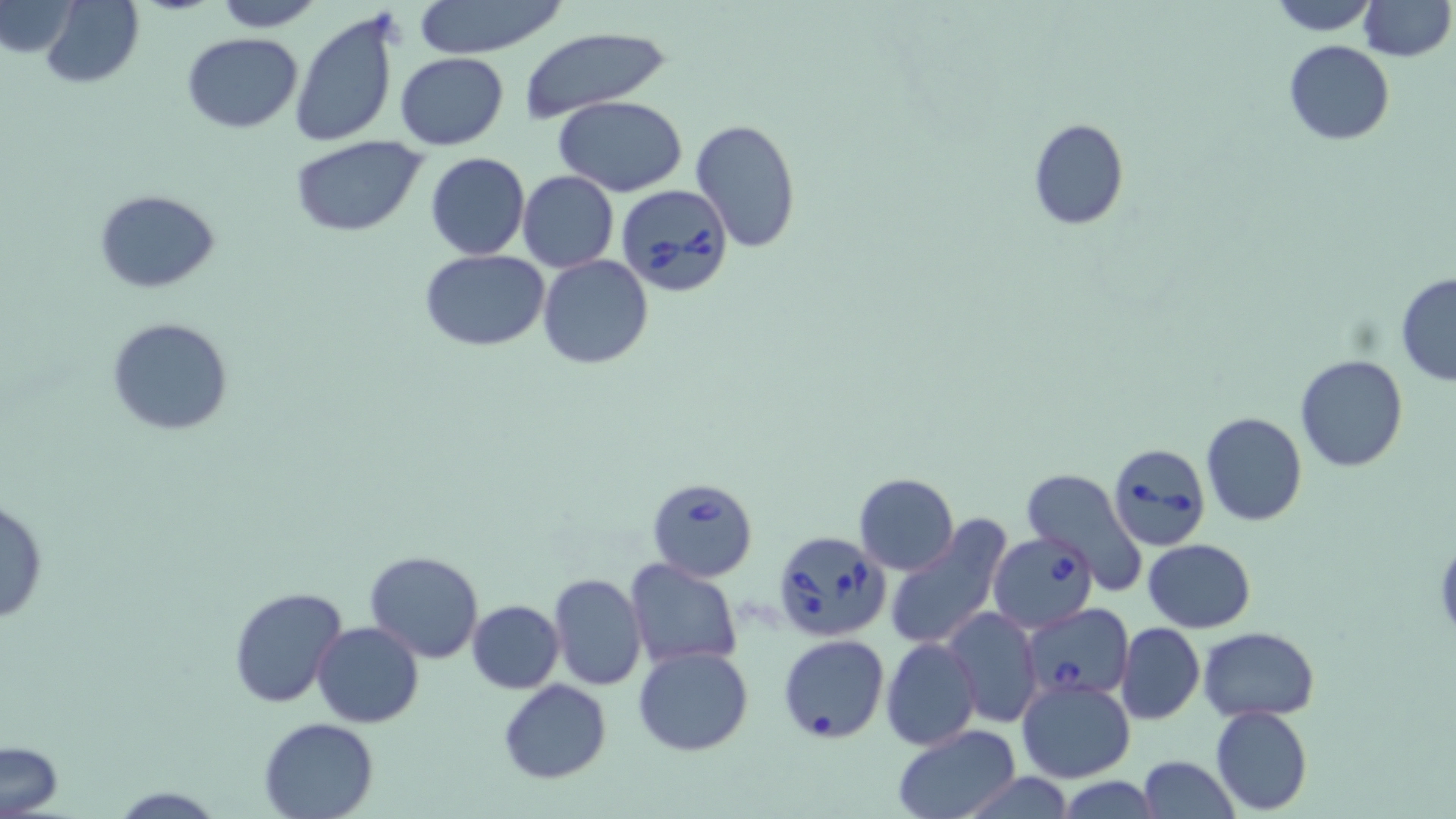

Approximate bounding boxes as named x1/y1/x2/y2 corners in pixels. Babesia divergens-infected red blood cell locations: (x1=614, y1=184, x2=734, y2=297), (x1=1107, y1=442, x2=1210, y2=551), (x1=646, y1=477, x2=758, y2=580), (x1=772, y1=529, x2=890, y2=641), (x1=987, y1=531, x2=1099, y2=634), (x1=1025, y1=602, x2=1137, y2=699). Uninfected red blood cell locations: (x1=0, y1=0, x2=78, y2=59), (x1=40, y1=0, x2=143, y2=89), (x1=210, y1=0, x2=325, y2=31), (x1=411, y1=0, x2=570, y2=58), (x1=1264, y1=0, x2=1380, y2=35), (x1=1357, y1=0, x2=1453, y2=61), (x1=289, y1=11, x2=400, y2=149), (x1=519, y1=29, x2=666, y2=119), (x1=183, y1=32, x2=302, y2=132), (x1=1282, y1=40, x2=1395, y2=145), (x1=395, y1=51, x2=509, y2=150), (x1=554, y1=96, x2=689, y2=198), (x1=1027, y1=117, x2=1128, y2=231), (x1=690, y1=118, x2=802, y2=252), (x1=290, y1=138, x2=425, y2=235), (x1=425, y1=151, x2=530, y2=259), (x1=518, y1=170, x2=620, y2=273), (x1=94, y1=191, x2=221, y2=292), (x1=419, y1=249, x2=550, y2=349), (x1=538, y1=254, x2=653, y2=369), (x1=1395, y1=275, x2=1456, y2=385), (x1=107, y1=317, x2=234, y2=437), (x1=1296, y1=356, x2=1407, y2=473), (x1=1201, y1=412, x2=1308, y2=527), (x1=1020, y1=469, x2=1148, y2=589), (x1=853, y1=473, x2=959, y2=574), (x1=0, y1=498, x2=49, y2=628), (x1=883, y1=517, x2=1012, y2=653), (x1=1435, y1=535, x2=1456, y2=644), (x1=1142, y1=539, x2=1255, y2=633), (x1=365, y1=549, x2=484, y2=664), (x1=625, y1=560, x2=742, y2=670), (x1=548, y1=573, x2=647, y2=691), (x1=227, y1=586, x2=348, y2=708), (x1=466, y1=598, x2=564, y2=693), (x1=942, y1=607, x2=1042, y2=729), (x1=312, y1=621, x2=423, y2=728), (x1=1117, y1=623, x2=1204, y2=724), (x1=1198, y1=627, x2=1321, y2=721), (x1=777, y1=633, x2=890, y2=744), (x1=882, y1=637, x2=981, y2=752), (x1=632, y1=645, x2=754, y2=755), (x1=1017, y1=677, x2=1135, y2=784), (x1=497, y1=680, x2=613, y2=784), (x1=1209, y1=705, x2=1312, y2=815), (x1=258, y1=716, x2=380, y2=819), (x1=890, y1=724, x2=1023, y2=819), (x1=1, y1=741, x2=65, y2=815), (x1=1137, y1=756, x2=1238, y2=817), (x1=111, y1=784, x2=223, y2=818). Slide-level diagnosis: Babesia divergens. Light microscopy. 1000x magnification. Thin blood smear. Image is 1456×819 pixels. May-Grünwald-Giemsa-stained preparation. Single field of view.